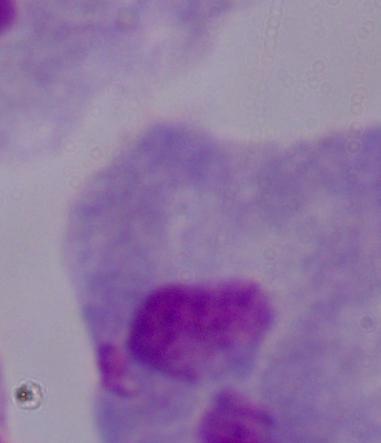

magnification: 1000x
modality: photomicrograph
identification: trichomonad